Comment on the morphology of the red blood cells.
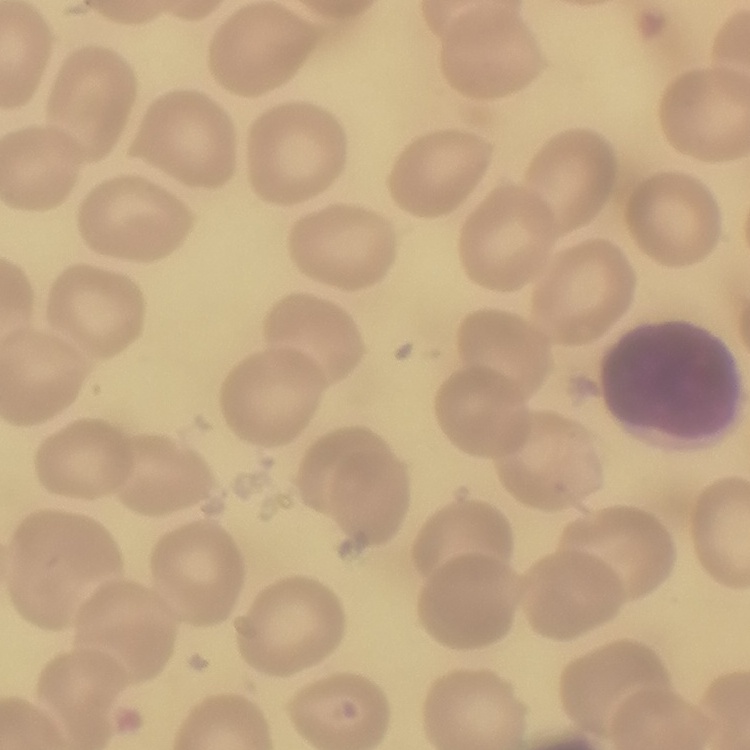
They show no rouleaux formation.

preparation: thin blood film
stain: Field's or Giemsa
image_type: square crop of a larger photomicrograph